Classify this cell by malaria status.
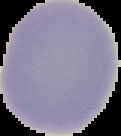

It is uninfected.

From a thin blood smear. Segmented cell region on a black background. Image is 121×136 pixels.